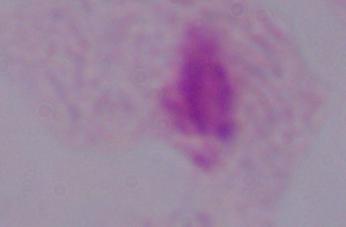

modality = photomicrograph
magnification = 1000x
identification = trichomonad